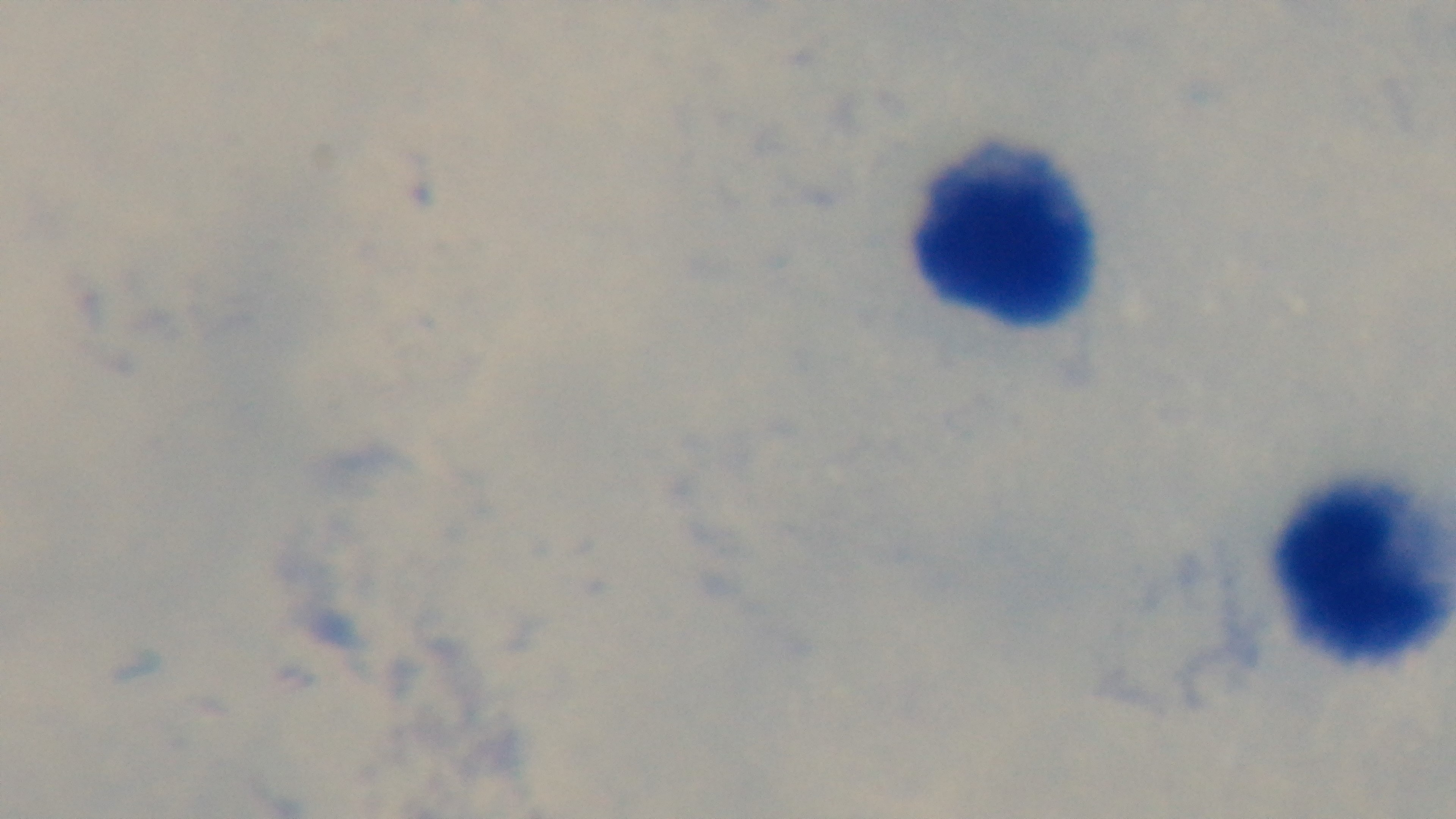

field of view = one from the slide
objective = 100x oil immersion
modality = light microscopy
preparation = thick blood film
stain = Giemsa
malaria status = negative
capture = mounted 4K digital camera